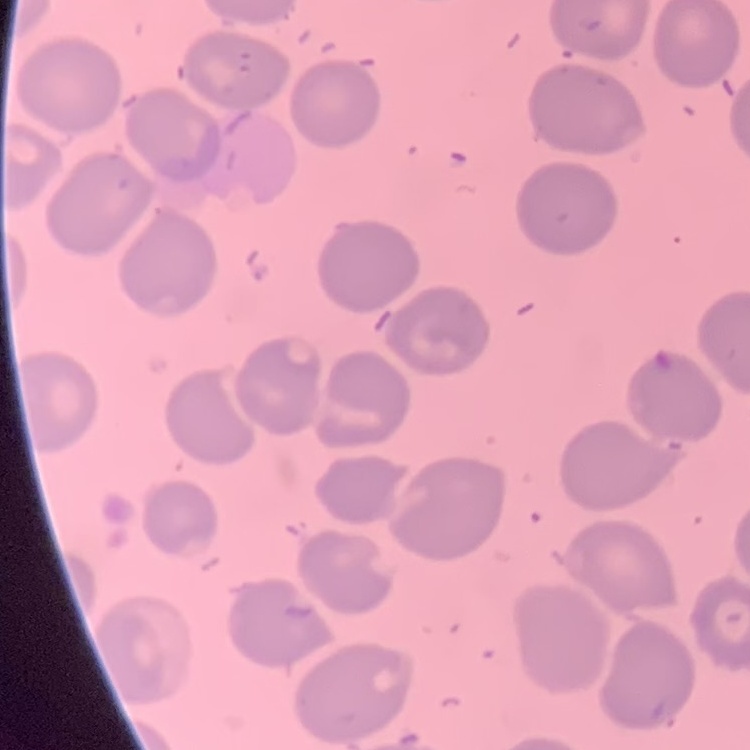

Summary:
  - Red blood cell morphology: no rouleaux formation
  - Stain: Field's or Giemsa
  - Image type: square crop of a larger photomicrograph
  - Preparation: thin blood film